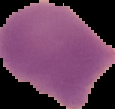
preparation = thin blood smear
image type = segmented cell region on a black background
malaria status = parasitized
image size = 115×109 pixels